Locate every parasitized red blood cell.
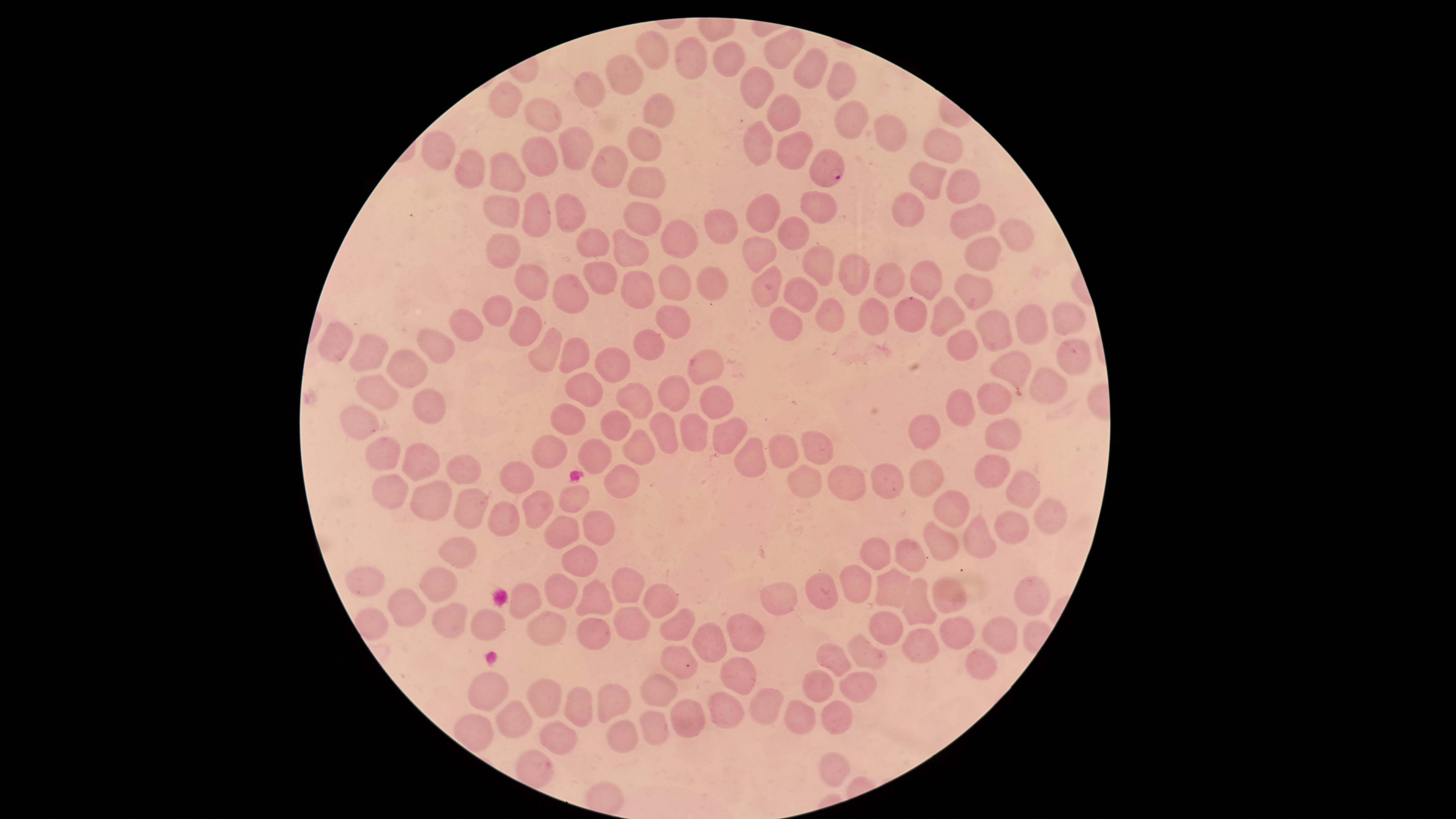
Approximate marker points, in pixels from the top-left corner.
Parasitized red blood cells: (x=830, y=168).

{
  "image_size": "1456×819 pixels",
  "field_of_view": "single",
  "preparation": "thin smear of blood",
  "species": "Plasmodium falciparum",
  "capture": "smartphone photograph through the microscope eyepiece",
  "stain": "Giemsa",
  "uninfected_red_blood_cells": "approximate marker points, in pixels from the top-left corner: (x=782, y=46), (x=657, y=47), (x=725, y=56), (x=685, y=63), (x=815, y=68), (x=622, y=75), (x=837, y=81), (x=761, y=85), (x=587, y=88), (x=509, y=103), (x=657, y=105), (x=781, y=109), (x=545, y=116), (x=851, y=122), (x=890, y=129), (x=759, y=140), (x=649, y=143), (x=433, y=148), (x=792, y=149), (x=937, y=149), (x=539, y=159), (x=575, y=159), (x=469, y=165), (x=608, y=169), (x=505, y=170), (x=922, y=176), (x=647, y=179), (x=958, y=182), (x=570, y=209), (x=821, y=210), (x=504, y=211), (x=769, y=212), (x=913, y=212), (x=539, y=217), (x=644, y=218), (x=968, y=219), (x=722, y=225), (x=797, y=228), (x=1012, y=230), (x=678, y=240), (x=596, y=242), (x=634, y=248), (x=504, y=250), (x=761, y=250), (x=981, y=258), (x=821, y=267), (x=858, y=275), (x=601, y=278), (x=533, y=279), (x=892, y=279), (x=930, y=279), (x=714, y=281), (x=767, y=284), (x=639, y=286), (x=672, y=286), (x=967, y=287), (x=572, y=293), (x=802, y=295), (x=496, y=307), (x=948, y=312), (x=829, y=314), (x=904, y=319), (x=1064, y=319), (x=872, y=320), (x=1030, y=323), (x=672, y=324), (x=784, y=324), (x=528, y=326), (x=472, y=328), (x=994, y=328), (x=651, y=339), (x=334, y=341), (x=428, y=343), (x=964, y=344), (x=368, y=349), (x=544, y=351), (x=578, y=355), (x=1066, y=358), (x=616, y=364), (x=404, y=367), (x=706, y=369), (x=1012, y=370), (x=585, y=385), (x=1051, y=385), (x=373, y=393), (x=670, y=396), (x=636, y=398), (x=719, y=400), (x=428, y=403), (x=994, y=403), (x=965, y=404), (x=566, y=420), (x=613, y=421), (x=361, y=422), (x=925, y=432), (x=1003, y=432), (x=662, y=433), (x=732, y=434), (x=695, y=437), (x=594, y=443), (x=821, y=443), (x=636, y=444), (x=546, y=446), (x=785, y=450), (x=387, y=451), (x=411, y=457), (x=759, y=457), (x=988, y=469), (x=517, y=471), (x=463, y=473), (x=623, y=479), (x=809, y=480), (x=882, y=481), (x=851, y=482), (x=924, y=484), (x=391, y=487), (x=1018, y=492), (x=573, y=497), (x=431, y=501), (x=532, y=507), (x=950, y=509), (x=469, y=510), (x=1047, y=515), (x=507, y=518), (x=594, y=524), (x=1010, y=525), (x=565, y=531), (x=938, y=541), (x=976, y=542), (x=876, y=552), (x=454, y=553), (x=905, y=558), (x=574, y=566), (x=628, y=577), (x=855, y=578), (x=897, y=580), (x=434, y=581), (x=373, y=586), (x=817, y=588), (x=559, y=593), (x=1035, y=593), (x=526, y=598), (x=951, y=598), (x=662, y=600), (x=592, y=603), (x=775, y=603), (x=918, y=606), (x=405, y=611), (x=630, y=614), (x=447, y=619), (x=489, y=624), (x=552, y=625), (x=884, y=626), (x=678, y=627), (x=1000, y=630), (x=590, y=631), (x=953, y=634), (x=741, y=638), (x=705, y=648), (x=917, y=648), (x=872, y=652), (x=832, y=657), (x=981, y=660), (x=677, y=663), (x=734, y=676), (x=816, y=684), (x=854, y=686), (x=489, y=691), (x=544, y=691), (x=662, y=691), (x=578, y=700), (x=617, y=701), (x=764, y=705), (x=722, y=711), (x=793, y=714), (x=837, y=715), (x=509, y=720), (x=687, y=725), (x=660, y=729), (x=564, y=731), (x=622, y=738), (x=535, y=766), (x=828, y=771)",
  "visible_region": "circular"
}